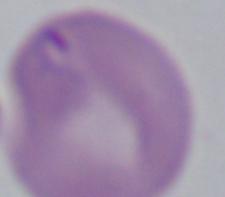
Micrograph. 1000x magnification. A Babesia parasite is seen.